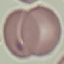

Summary:
  - Malaria status: uninfected
  - Stain: Giemsa
  - Preparation: thin blood film
  - Capture: smartphone through the microscope eyepiece
  - Image type: cell patch, automatically extracted from a larger field of view and resized to 64 × 64 pixels